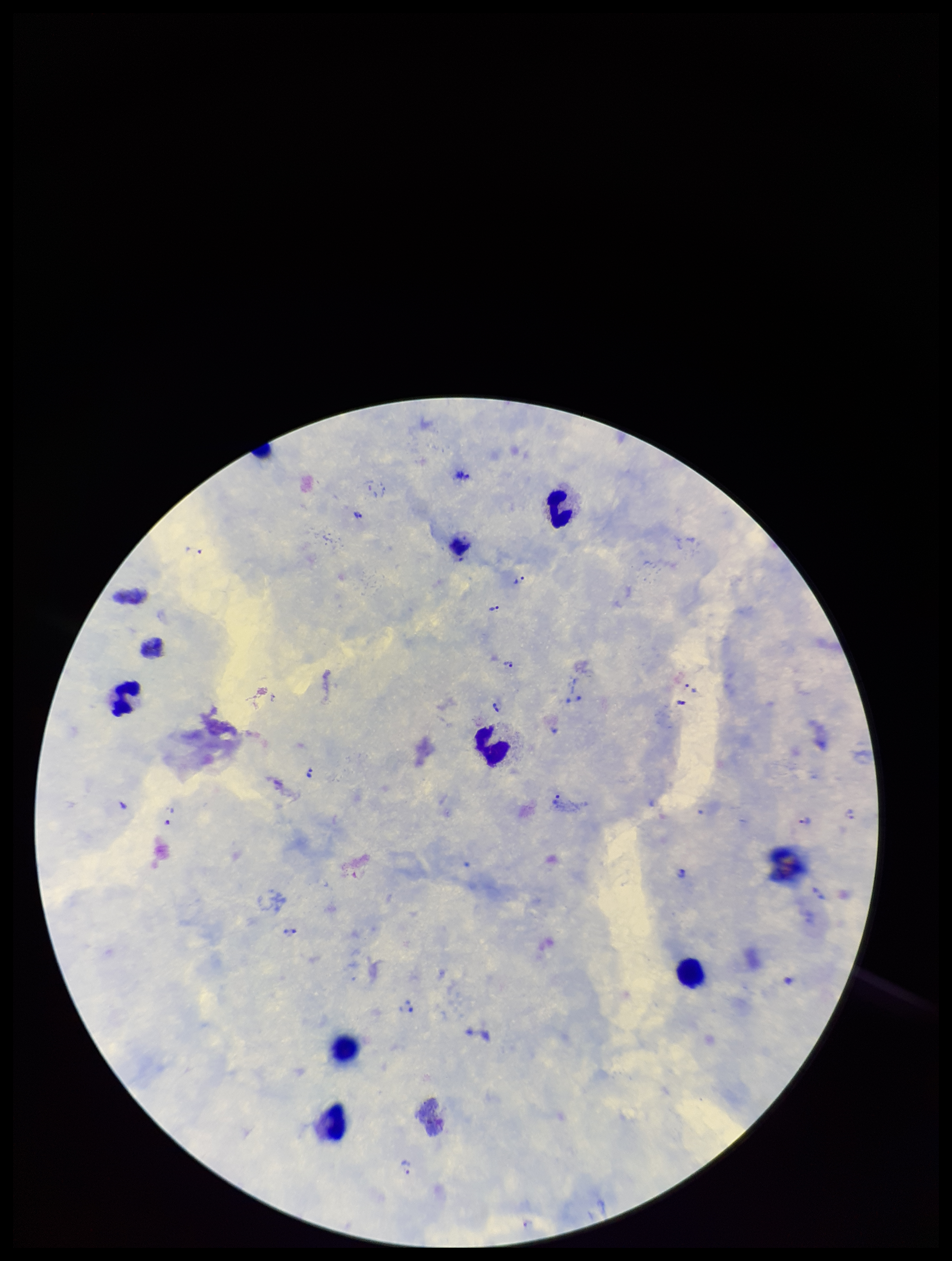

image size = 952×1261 pixels
capture = smartphone photograph through the microscope eyepiece
Plasmodium parasites = identified
leukocyte count = 7
patient malaria status = positive
species reported for this patient = Plasmodium vivax
parasite count = 22
stain = Giemsa
preparation = thick blood smear
field of view = one from this slide